Report the malaria status of this cell.
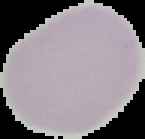
It is uninfected.

Summary:
  - Image size: 145×139 pixels
  - Preparation: thin blood film
  - Image type: cell region segmented out of the field of view; surrounding area masked to black